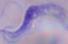

modality = photomicrograph
magnification = 1000x
identification = trypanosome